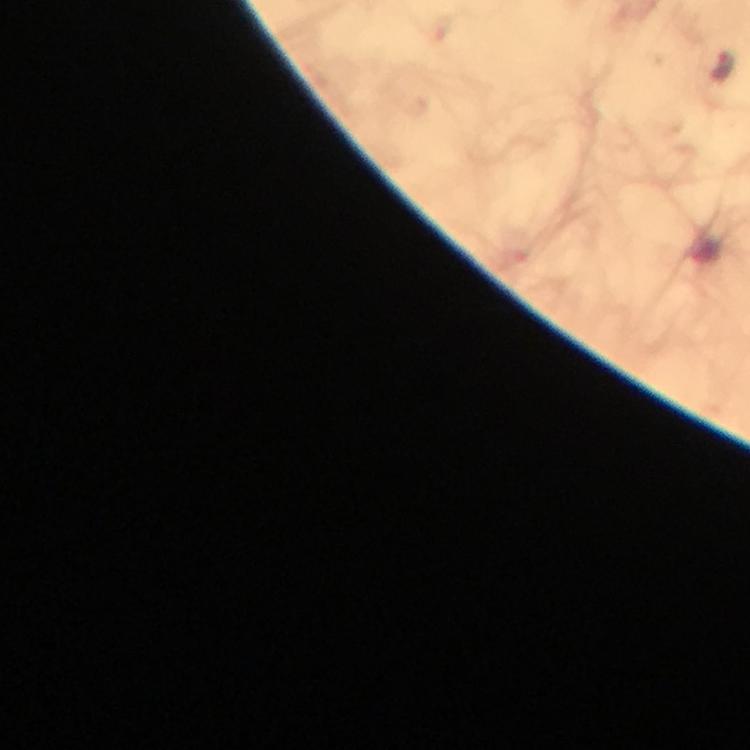

Plasmodium parasite locations = approximate centers as (x, y) in pixels: (722, 67)
magnification = 100x
context = from a malaria diagnostic workup
stain = Giemsa
preparation = thick smear
capture = smartphone mounted on the microscope
cropped from = one field of view
image size = 750×750 pixels
immersion oil = applied